Report the malaria status of this cell.
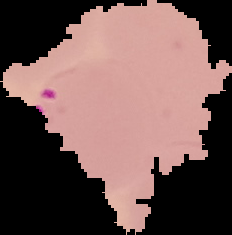

It is parasitized.

Image is 232×235 pixels. From a thin blood film. Segmented cell region on a black background.